Locate every P. falciparum parasite and give its life-cycle stage, and locate every leukocyte and any debris.
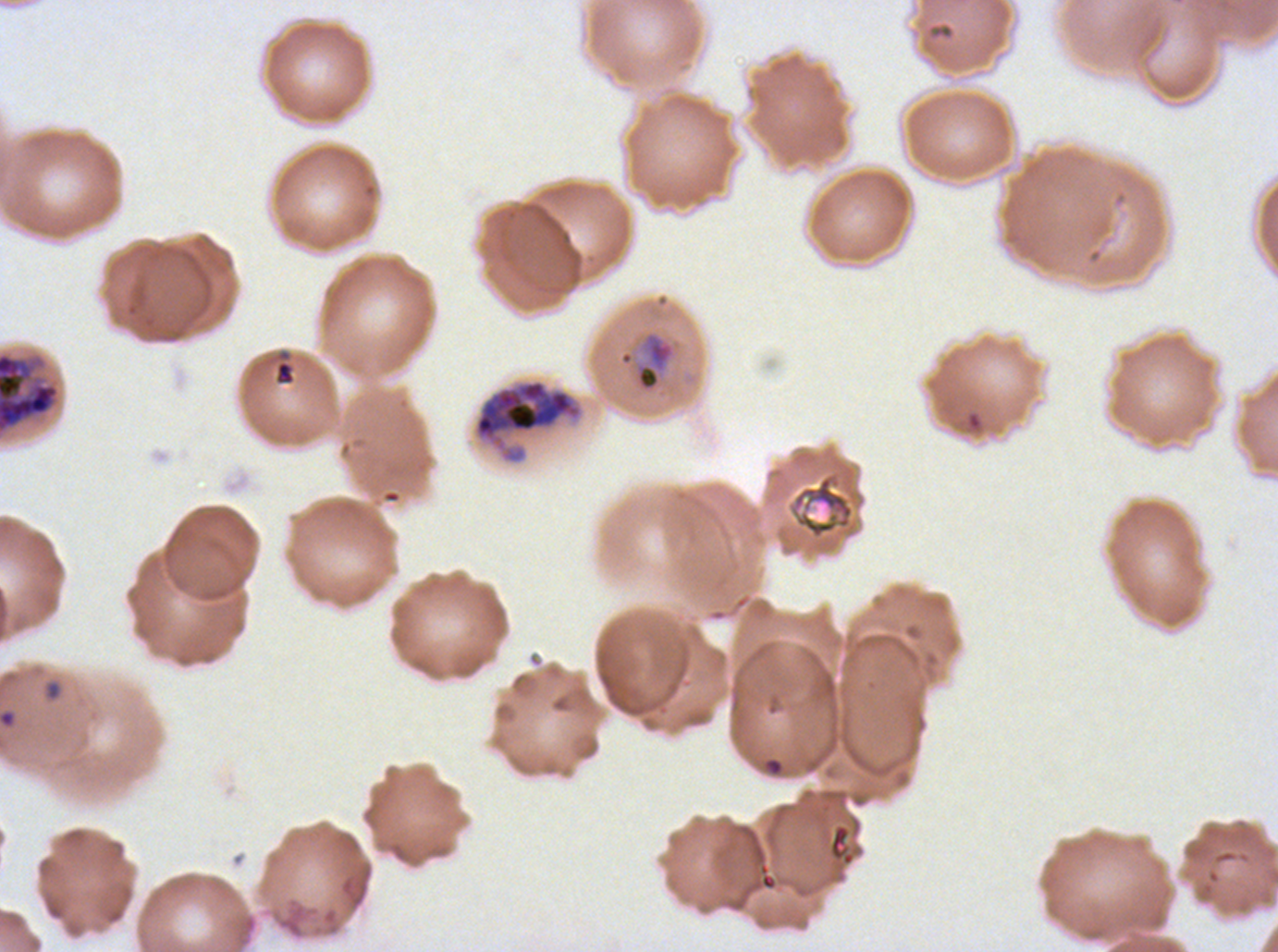

Approximate bounding boxes as (x1, y1, x2, y2) in pixels.
Rings: (42, 677, 64, 703).
Mid trophozoites: (633, 330, 677, 394).
Late trophozoites: (0, 351, 61, 436).
Late schizonts: (474, 380, 578, 439).
Debris: (273, 348, 297, 386), (788, 470, 857, 540).
No late-ring/early-trophozoite forms, early schizonts, segmenters, gametocytes, or leukocytes observed.

stain = Giemsa
field of view = sub-image separated from a larger composite
life-cycle stages observed = ring, mid trophozoite, late trophozoite, late schizont
preparation = thin blood film
specimen = P. falciparum from a patient in The Gambia, cultured ex vivo for 24 to 48 hours
image size = 1278×952 pixels